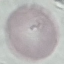

result = no malaria parasites detected
capture = smartphone through the microscope eyepiece
image type = cell patch, automatically extracted from a larger field of view and resized to 64 × 64 pixels
preparation = thin blood film
stain = Giemsa